Give the position of every leukocyte visible.
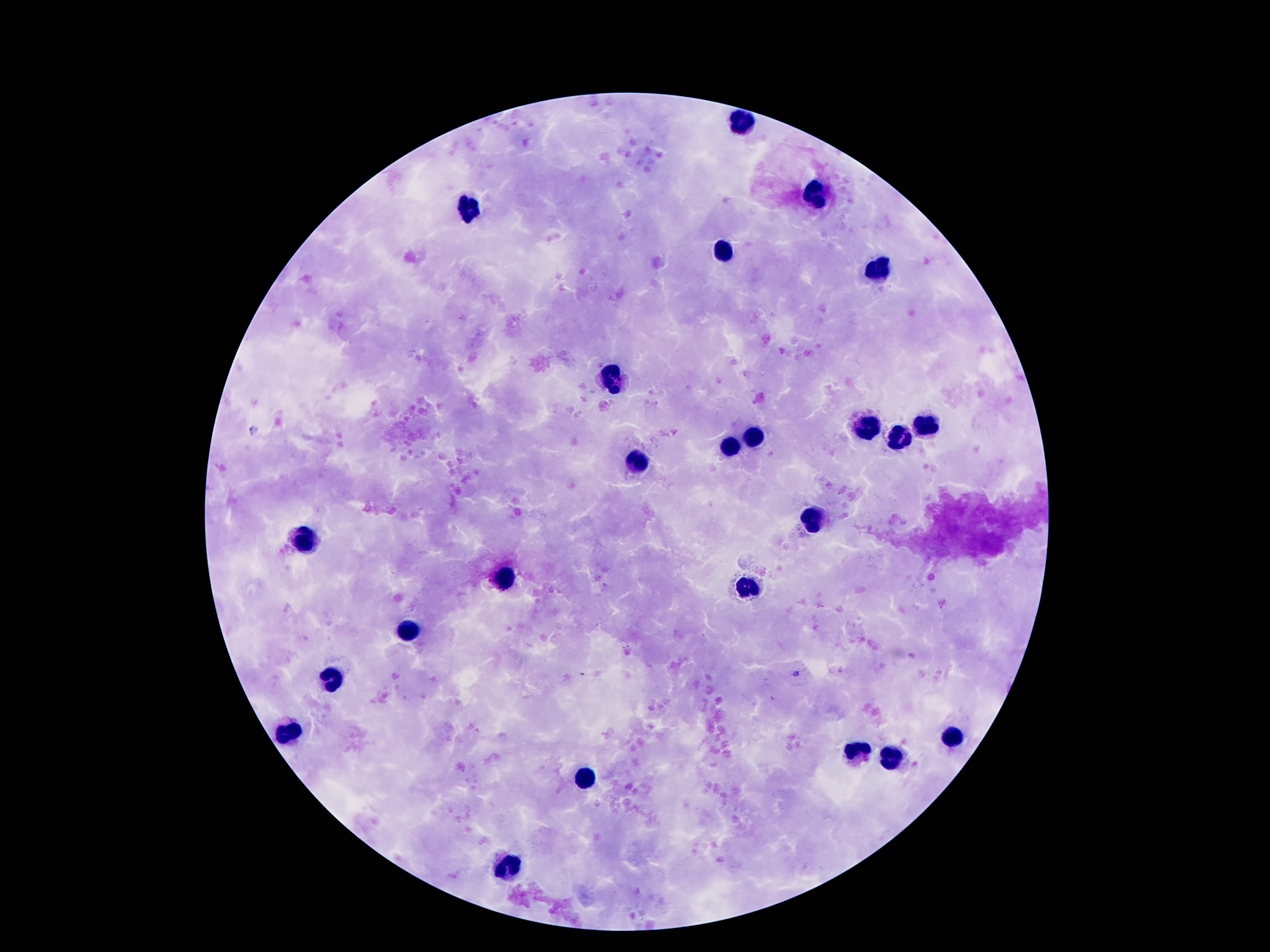

Approximate object centers, in pixels from the top-left corner.
Leukocytes: (x=743, y=121), (x=815, y=193), (x=467, y=209), (x=723, y=253), (x=877, y=269), (x=613, y=377), (x=925, y=425), (x=867, y=431), (x=755, y=439), (x=893, y=441), (x=727, y=445), (x=635, y=461), (x=811, y=519), (x=305, y=541), (x=503, y=579), (x=751, y=587), (x=407, y=628), (x=333, y=676), (x=289, y=731), (x=953, y=740), (x=861, y=751), (x=889, y=761), (x=583, y=781), (x=509, y=868).

stain = Giemsa
image size = 1270×952 pixels
field of view = single
magnification = 100x
patient malaria status = not infected
preparation = thick blood smear
capture = smartphone camera through the microscope eyepiece